Assess the morphology of the erythrocytes.
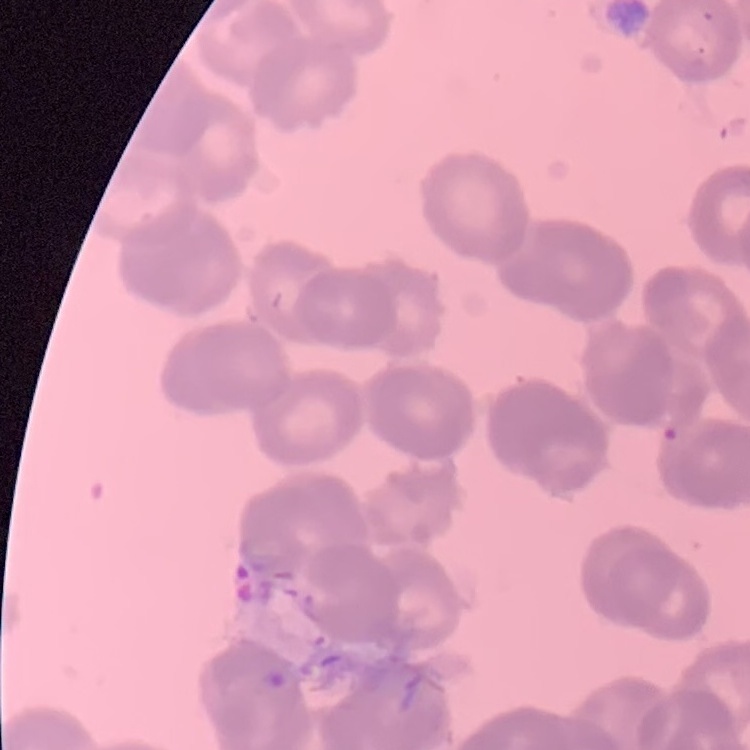

Rouleaux formation.

Summary:
  - Preparation: thin blood smear
  - Image type: square crop of a larger photomicrograph
  - Stain: Field's or Giemsa